Report the malaria status of this cell.
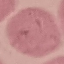
Uninfected.

capture = smartphone camera at the microscope eyepiece
stain = Giemsa
image type = cell patch, automatically extracted from a larger field of view and resized to 64 × 64 pixels
preparation = thin smear